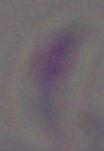
{
  "identification": "Toxoplasma gondii",
  "magnification": "1000x",
  "modality": "micrograph"
}